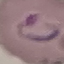 Malaria status: parasitized. Thin blood smear. Acquired by smartphone through the microscope eyepiece. Giemsa stain. Cell patch, automatically extracted from a larger field of view and resized to 64 × 64 pixels.